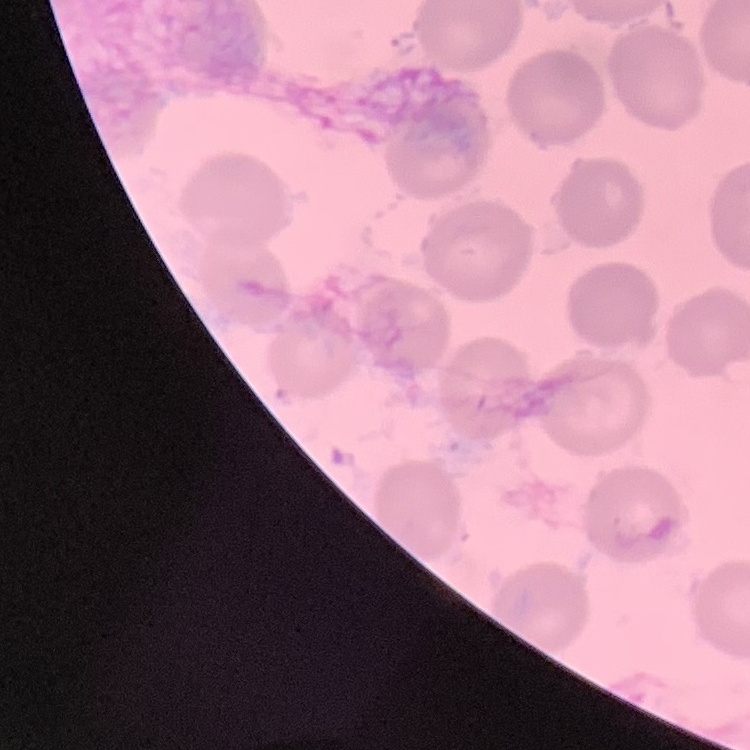
Summary:
  - Red blood cell morphology: no rouleaux formation
  - Image type: square crop of a larger photomicrograph
  - Preparation: thin blood smear
  - Stain: Field's or Giemsa